Name the parasite shown.
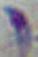
Toxoplasma gondii.

Summary:
  - Modality: photomicrograph
  - Magnification: 1000x